Locate every blood parasite and identify its species.
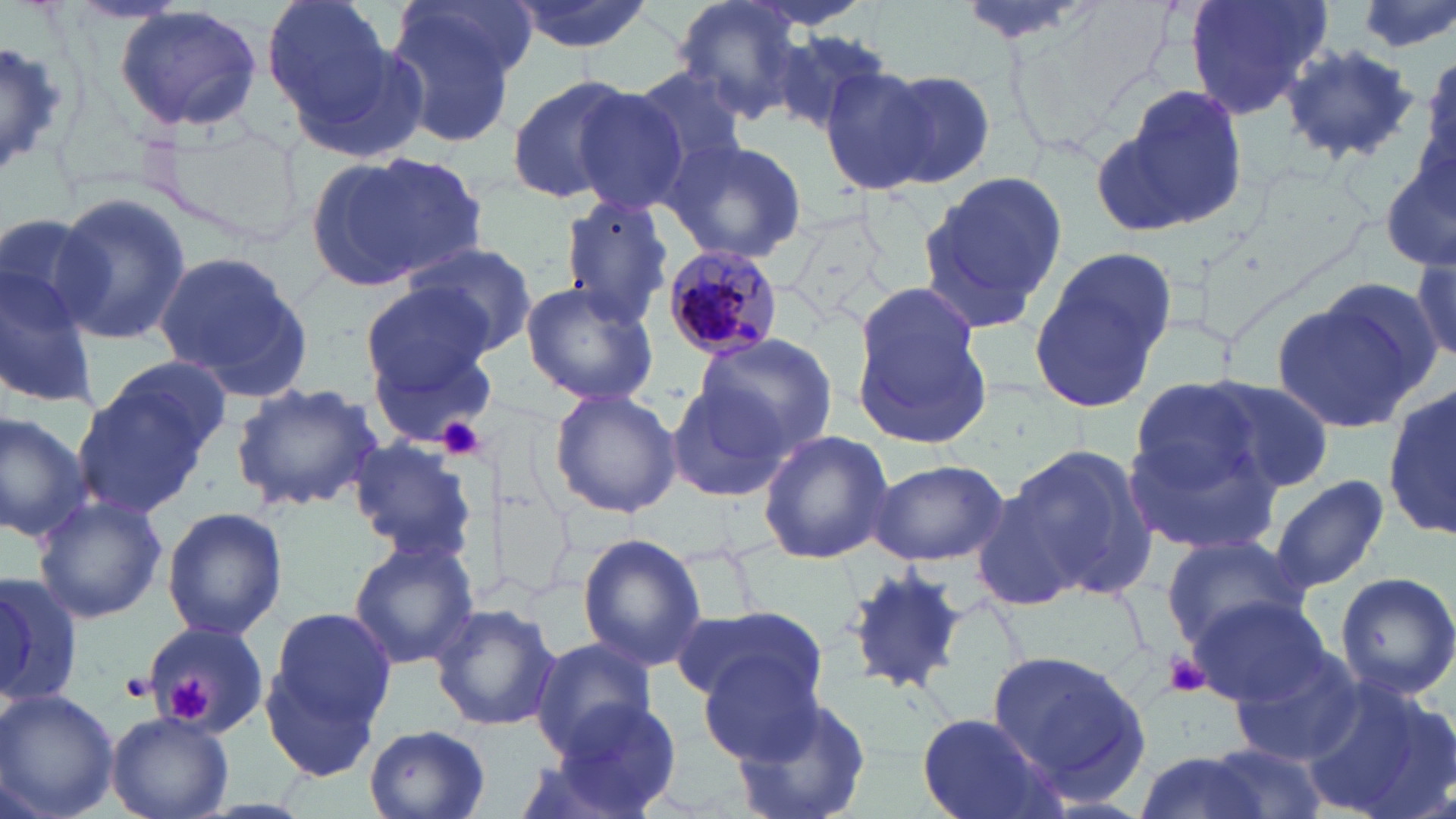
Approximate bounding boxes as named x1/y1/x2/y2 corners in pixels.
Plasmodium malariae-infected red blood cells: (x1=656, y1=244, x2=787, y2=359).
No Plasmodium falciparum, Plasmodium ovale, Plasmodium vivax, Babesia divergens, or Trypanosoma brucei observed.

Summary:
  - Uninfected red blood cell locations: (x1=261, y1=0, x2=404, y2=138), (x1=509, y1=0, x2=659, y2=54), (x1=744, y1=0, x2=881, y2=33), (x1=956, y1=0, x2=1097, y2=46), (x1=1186, y1=0, x2=1335, y2=123), (x1=1348, y1=0, x2=1456, y2=56), (x1=388, y1=1, x2=527, y2=136), (x1=673, y1=1, x2=818, y2=122), (x1=113, y1=4, x2=264, y2=134), (x1=768, y1=26, x2=896, y2=137), (x1=0, y1=37, x2=64, y2=180), (x1=1280, y1=43, x2=1422, y2=163), (x1=1421, y1=53, x2=1455, y2=184), (x1=625, y1=64, x2=751, y2=180), (x1=823, y1=65, x2=938, y2=196), (x1=875, y1=69, x2=998, y2=188), (x1=505, y1=74, x2=636, y2=205), (x1=1102, y1=81, x2=1249, y2=236), (x1=568, y1=82, x2=696, y2=215), (x1=662, y1=136, x2=808, y2=265), (x1=317, y1=151, x2=489, y2=291), (x1=1380, y1=152, x2=1456, y2=275), (x1=915, y1=171, x2=1068, y2=331), (x1=51, y1=191, x2=190, y2=348), (x1=558, y1=194, x2=674, y2=325), (x1=783, y1=207, x2=893, y2=331), (x1=0, y1=212, x2=109, y2=341), (x1=398, y1=239, x2=539, y2=356), (x1=1028, y1=247, x2=1178, y2=412), (x1=152, y1=252, x2=312, y2=397), (x1=0, y1=257, x2=97, y2=410), (x1=1412, y1=258, x2=1454, y2=362), (x1=1382, y1=261, x2=1456, y2=378), (x1=361, y1=281, x2=494, y2=394), (x1=519, y1=281, x2=660, y2=407), (x1=1273, y1=286, x2=1435, y2=433), (x1=851, y1=288, x2=990, y2=445), (x1=366, y1=332, x2=501, y2=448), (x1=694, y1=332, x2=839, y2=457), (x1=75, y1=360, x2=228, y2=519), (x1=1129, y1=374, x2=1280, y2=504), (x1=1197, y1=377, x2=1333, y2=495), (x1=230, y1=381, x2=384, y2=511), (x1=1386, y1=381, x2=1456, y2=548), (x1=663, y1=384, x2=791, y2=503), (x1=548, y1=388, x2=682, y2=519), (x1=0, y1=409, x2=92, y2=543), (x1=1123, y1=424, x2=1285, y2=559), (x1=758, y1=429, x2=894, y2=563), (x1=345, y1=436, x2=476, y2=565), (x1=1006, y1=442, x2=1164, y2=602), (x1=865, y1=458, x2=1008, y2=566), (x1=1269, y1=473, x2=1389, y2=593), (x1=970, y1=488, x2=1090, y2=611), (x1=33, y1=495, x2=166, y2=625), (x1=161, y1=505, x2=289, y2=642), (x1=578, y1=533, x2=707, y2=669), (x1=1158, y1=536, x2=1309, y2=653), (x1=348, y1=539, x2=479, y2=670), (x1=842, y1=563, x2=969, y2=696), (x1=1334, y1=569, x2=1456, y2=702), (x1=0, y1=576, x2=84, y2=706), (x1=1190, y1=597, x2=1332, y2=708), (x1=431, y1=602, x2=562, y2=731), (x1=265, y1=604, x2=399, y2=739), (x1=673, y1=604, x2=826, y2=712), (x1=143, y1=615, x2=271, y2=751), (x1=529, y1=637, x2=657, y2=756), (x1=988, y1=648, x2=1152, y2=806), (x1=258, y1=650, x2=386, y2=782), (x1=695, y1=650, x2=827, y2=766), (x1=1228, y1=650, x2=1367, y2=764), (x1=1301, y1=677, x2=1450, y2=819), (x1=0, y1=688, x2=119, y2=819), (x1=727, y1=692, x2=875, y2=819), (x1=544, y1=700, x2=687, y2=819), (x1=107, y1=710, x2=233, y2=818), (x1=914, y1=711, x2=1053, y2=818), (x1=366, y1=725, x2=491, y2=818), (x1=1203, y1=741, x2=1328, y2=819), (x1=1129, y1=749, x2=1279, y2=819)
  - Platelet locations: (x1=434, y1=412, x2=488, y2=460), (x1=1165, y1=652, x2=1209, y2=698), (x1=118, y1=672, x2=152, y2=702), (x1=165, y1=676, x2=213, y2=723)
  - Slide-level diagnosis: Plasmodium malariae
  - Field of view: one of a larger specimen
  - Magnification: 1000x
  - Image size: 1456×819 pixels
  - Stain: May-Grünwald-Giemsa
  - Modality: light microscopy
  - Preparation: thin blood film